Locate and identify every blood parasite.
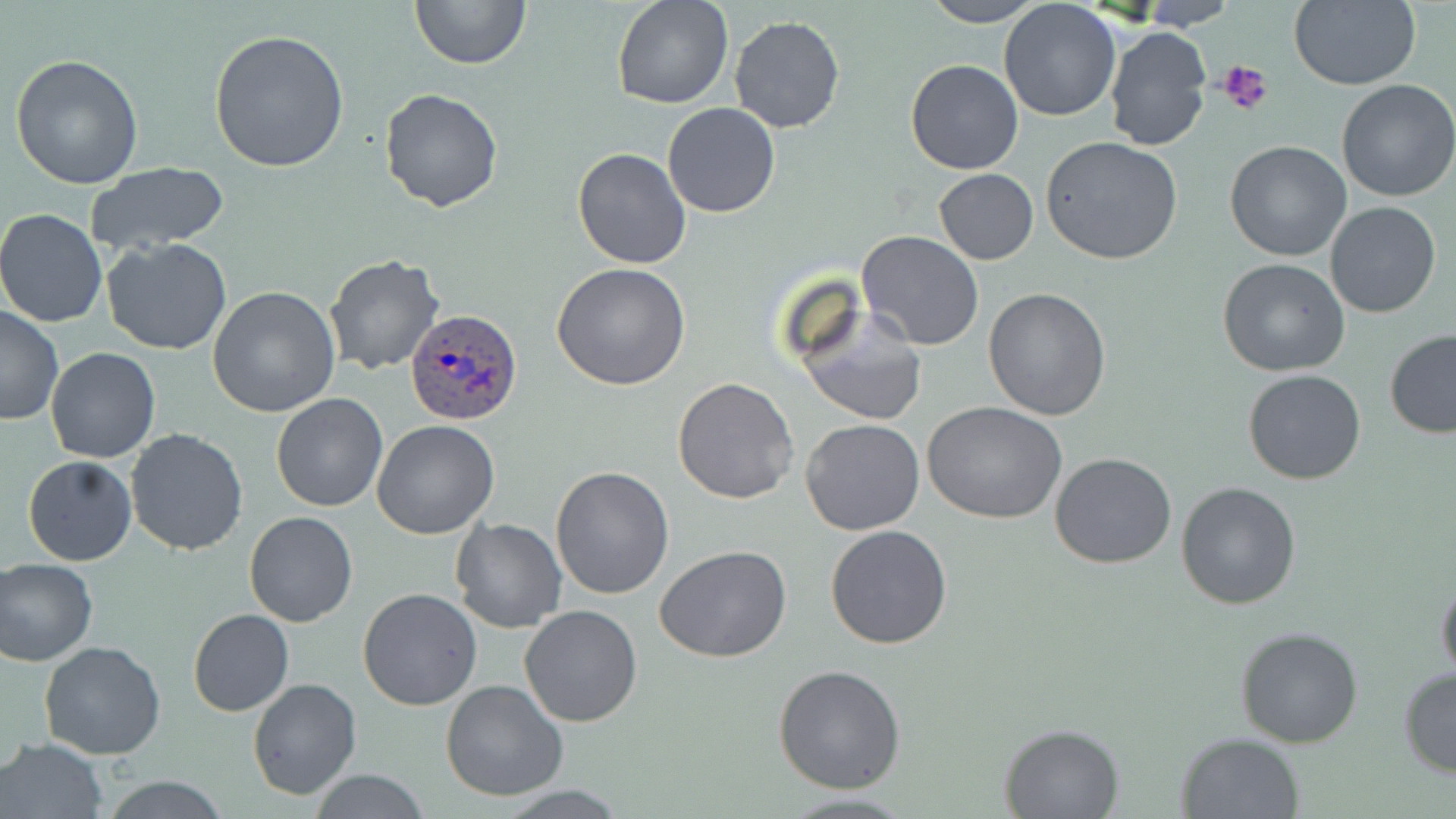

Approximate bounding boxes as (x1,y1)-(x2,y2) corner pairs in pixels.
Plasmodium ovale-infected red blood cells: (405,308)-(521,427).
No Plasmodium falciparum, Plasmodium malariae, Plasmodium vivax, Babesia divergens, or Trypanosoma brucei observed.

slide-level diagnosis = Plasmodium ovale
uninfected red blood cell locations = approximate bounding boxes as (x1,y1)-(x2,y2) corner pairs in pixels: (410,0)-(529,70), (611,0)-(733,109), (920,0)-(1046,26), (1290,0)-(1421,90), (998,1)-(1122,122), (1135,1)-(1237,30), (729,16)-(846,133), (1103,26)-(1211,153), (207,29)-(350,173), (9,54)-(145,190), (905,59)-(1023,175), (1336,80)-(1456,202), (379,87)-(505,211), (664,103)-(780,218), (590,110)-(743,241), (1040,137)-(1184,266), (1223,139)-(1351,262), (572,147)-(691,268), (85,161)-(229,256), (933,169)-(1039,265), (1324,202)-(1442,319), (0,209)-(107,328), (0,225)-(225,343), (857,231)-(984,350), (102,237)-(233,356), (323,252)-(447,376), (1218,258)-(1350,375), (551,263)-(693,392), (209,285)-(341,417), (983,286)-(1112,421), (795,304)-(926,427), (0,307)-(64,426), (1383,329)-(1456,438), (45,346)-(160,464), (1243,369)-(1367,485), (672,377)-(800,504), (271,393)-(387,511), (922,401)-(1067,523), (801,418)-(925,536), (370,420)-(500,539), (124,428)-(249,556), (1050,452)-(1178,569), (22,455)-(137,567), (551,465)-(675,598), (1176,481)-(1302,610), (244,511)-(357,627), (450,518)-(566,634), (824,524)-(953,649), (654,546)-(792,664), (1,558)-(97,666), (1436,572)-(1456,687), (358,588)-(484,711), (518,605)-(643,728), (188,608)-(293,715), (1235,627)-(1364,747), (38,639)-(167,759), (773,664)-(906,794), (1397,667)-(1456,778), (246,678)-(362,801), (440,680)-(568,803), (998,722)-(1126,817), (1174,732)-(1306,819), (2,736)-(107,818), (311,770)-(431,819), (99,776)-(233,817), (488,784)-(633,816), (771,790)-(920,818)
modality = light microscopy
magnification = 1000x
image size = 1456×819 pixels
field of view = single
preparation = thin blood film
stain = May-Grünwald-Giemsa
platelet locations = approximate bounding boxes as (x1,y1)-(x2,y2) corner pairs in pixels: (1218,60)-(1273,118)